Classify this cell by malaria status.
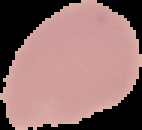

It is uninfected.

Summary:
  - Preparation: thin blood smear
  - Image type: cell region segmented out of the field of view; surrounding area masked to black
  - Image size: 142×130 pixels